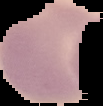

From a thin blood smear. The area outside the segmented cell region is set to black. Result: no malaria parasites detected. Image is 103×106 pixels.